Classify this cell by malaria status.
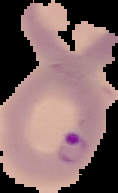
Parasitized.

Image is 118×193 pixels. From a thin blood smear. Segmented cell region on a black background.